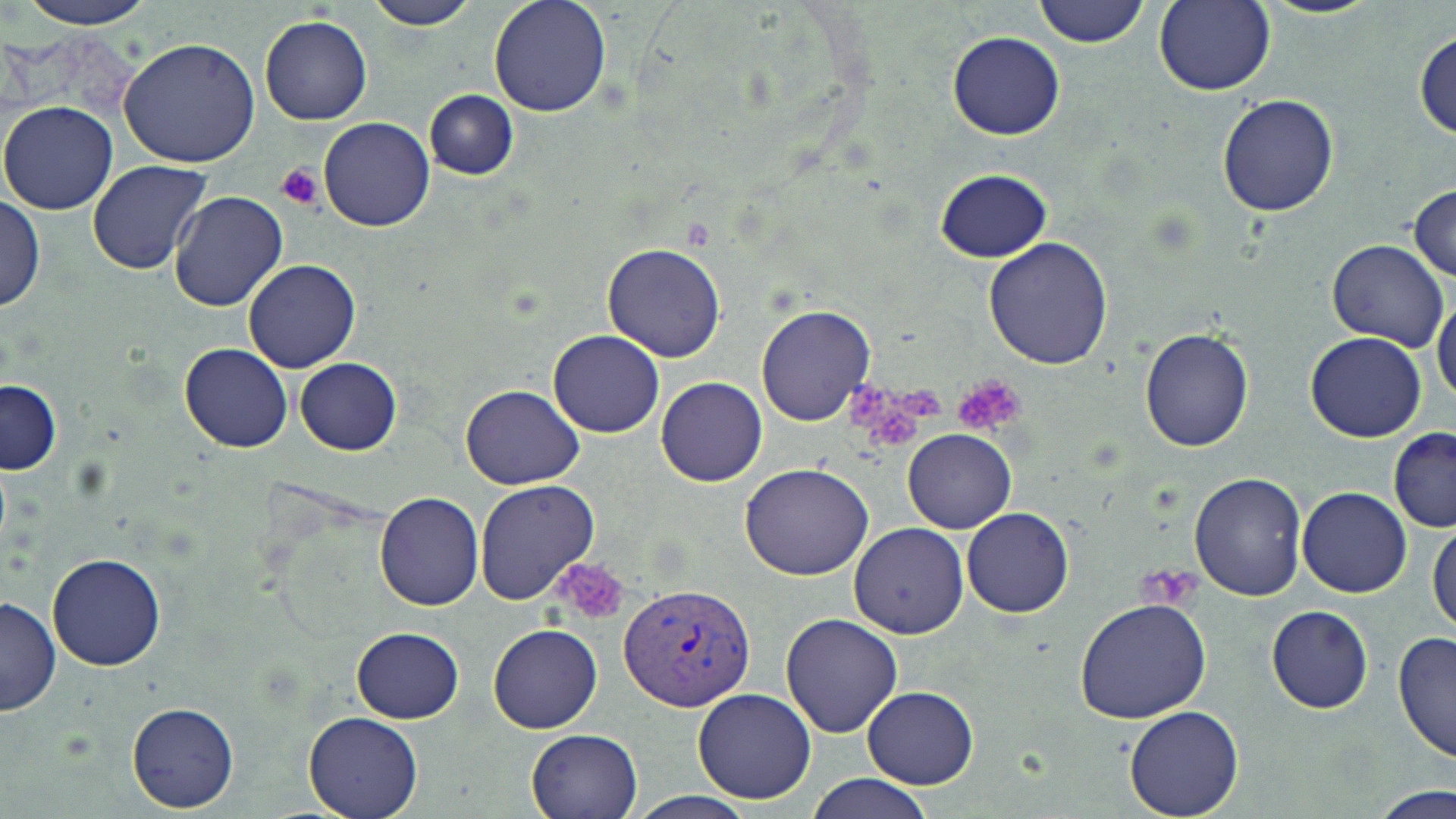

slide_level_diagnosis: Plasmodium vivax
platelet_locations: 'approximate bounding boxes as (x1, y1, x2, y2) in pixels: (275, 164, 325, 210), (952, 374, 1026, 435), (847, 380, 941, 449), (548, 557, 632, 625), (1141, 567, 1197, 608)'
image_size: 1456×819 pixels
field_of_view: single
stain: May-Grünwald-Giemsa
preparation: thin blood film
plasmodium_vivax_infected_red_blood_cell_locations: 'approximate bounding boxes as (x1, y1, x2, y2) in pixels: (615, 588, 756, 712)'
magnification: 1000x
modality: light microscopy
uninfected_red_blood_cell_locations: 'approximate bounding boxes as (x1, y1, x2, y2) in pixels: (12, 0, 159, 29), (364, 0, 477, 29), (488, 0, 613, 117), (1033, 0, 1147, 46), (1259, 0, 1382, 21), (1153, 1, 1275, 97), (259, 15, 372, 125), (1413, 27, 1456, 145), (947, 31, 1064, 141), (118, 39, 262, 170), (423, 89, 517, 180), (1217, 93, 1340, 217), (0, 101, 119, 215), (318, 117, 435, 232), (87, 159, 214, 277), (934, 168, 1053, 262), (1408, 183, 1456, 283), (167, 191, 288, 311), (1, 194, 44, 314), (983, 238, 1114, 371), (1328, 238, 1450, 352), (602, 244, 726, 363), (242, 258, 361, 373), (1432, 294, 1456, 410), (754, 305, 876, 427), (1138, 327, 1254, 451), (547, 330, 665, 437), (1304, 332, 1428, 442), (179, 342, 293, 453), (295, 358, 402, 455), (656, 377, 767, 487), (0, 379, 60, 474), (460, 384, 583, 490), (902, 428, 1016, 533), (1387, 429, 1456, 534), (741, 464, 874, 581), (1189, 471, 1307, 601), (475, 481, 600, 604), (1297, 488, 1411, 598), (374, 491, 484, 611), (962, 506, 1073, 617), (1428, 521, 1456, 636), (848, 523, 968, 639), (45, 553, 167, 671), (0, 596, 60, 717), (1075, 599, 1210, 722), (1265, 605, 1373, 714), (780, 612, 904, 737), (487, 624, 601, 733), (350, 626, 464, 724), (1393, 633, 1455, 763), (861, 685, 980, 790), (692, 688, 817, 803), (125, 702, 238, 813), (1123, 706, 1245, 819), (302, 712, 423, 819), (527, 728, 643, 819), (805, 773, 934, 818), (1363, 783, 1456, 818), (626, 791, 759, 819)'